Outline each Plasmodium falciparum-infected red blood cell.
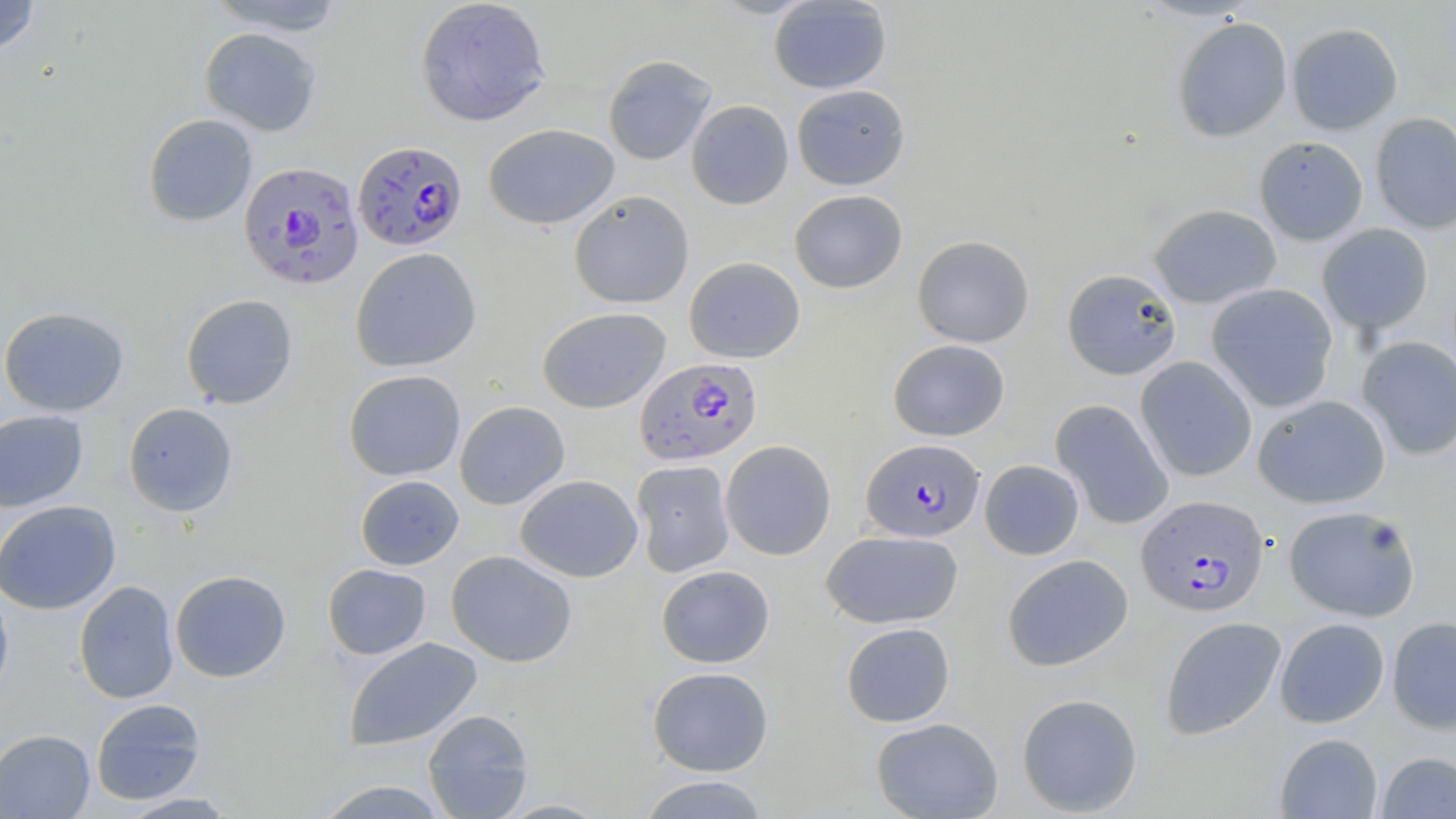
Approximate bounding boxes as (x1,y1)-(x2,y2) corner pairs in pixels.
Plasmodium falciparum-infected red blood cells: (353,140)-(467,252), (238,161)-(364,290), (635,356)-(762,466), (861,438)-(985,542), (1137,494)-(1268,616).

slide_level_diagnosis: Plasmodium falciparum
field_of_view: single
magnification: 1000x
image_size: 1456×819 pixels
preparation: thin blood film
uninfected_red_blood_cell_locations: 'approximate bounding boxes as (x1,y1)-(x2,y2) corner pairs in pixels: (0,0)-(40,56), (204,0)-(350,35), (415,0)-(551,126), (768,0)-(892,94), (1171,16)-(1293,142), (1286,22)-(1403,135), (199,27)-(322,136), (602,54)-(717,166), (792,84)-(910,190), (686,99)-(794,210), (1370,112)-(1456,234), (142,113)-(258,227), (483,124)-(620,230), (1253,136)-(1369,246), (789,189)-(907,293), (569,191)-(694,309), (1148,203)-(1282,309), (1316,223)-(1434,336), (912,234)-(1035,347), (350,247)-(482,372), (684,256)-(805,363), (1062,268)-(1182,380), (1206,283)-(1338,412), (180,294)-(298,410), (0,306)-(130,417), (537,306)-(671,413), (1356,337)-(1456,459), (888,339)-(1010,441), (1135,356)-(1257,482), (343,369)-(466,481), (1253,394)-(1390,509), (1050,399)-(1175,530), (454,401)-(570,510), (123,402)-(238,517), (0,409)-(89,512), (720,440)-(836,560), (979,459)-(1084,560), (631,460)-(735,577), (515,474)-(643,582), (355,475)-(464,570), (0,500)-(121,615), (1283,504)-(1421,621), (821,529)-(963,629), (446,550)-(578,668), (1002,554)-(1134,671), (322,564)-(432,660), (656,565)-(775,668), (170,570)-(291,683), (0,580)-(15,708), (73,580)-(180,704), (1160,616)-(1286,740), (1387,616)-(1456,734), (1275,617)-(1390,727), (841,622)-(955,727), (343,637)-(483,752), (647,666)-(774,776), (1016,693)-(1143,816), (90,698)-(206,805), (422,708)-(534,819), (871,717)-(1004,818), (0,729)-(95,818), (1275,733)-(1383,818), (1376,751)-(1456,818), (636,774)-(772,819), (311,779)-(453,818), (116,792)-(240,818), (495,798)-(612,818)'
modality: light microscopy
stain: May-Grünwald-Giemsa